Comment on the morphology of the erythrocytes.
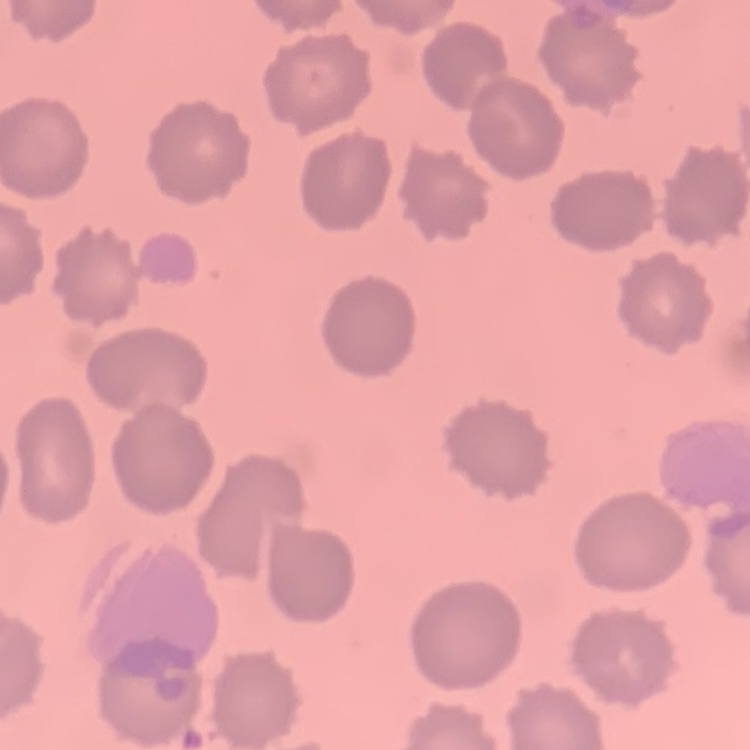

No rouleaux formation.

preparation = thin peripheral smear
image type = square crop of a larger photomicrograph
stain = Field's or Giemsa